Report the malaria status of this cell.
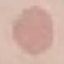

It is uninfected.

Photographed with a smartphone camera at the microscope eyepiece. Giemsa stain. Thin blood smear. Cell patch, automatically extracted from a larger field of view and resized to 64 × 64 pixels.